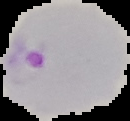

Summary:
  - Image type: segmented cell region with the area outside set to black
  - Result: Plasmodium parasites identified
  - Image size: 130×121 pixels
  - Preparation: thin blood smear